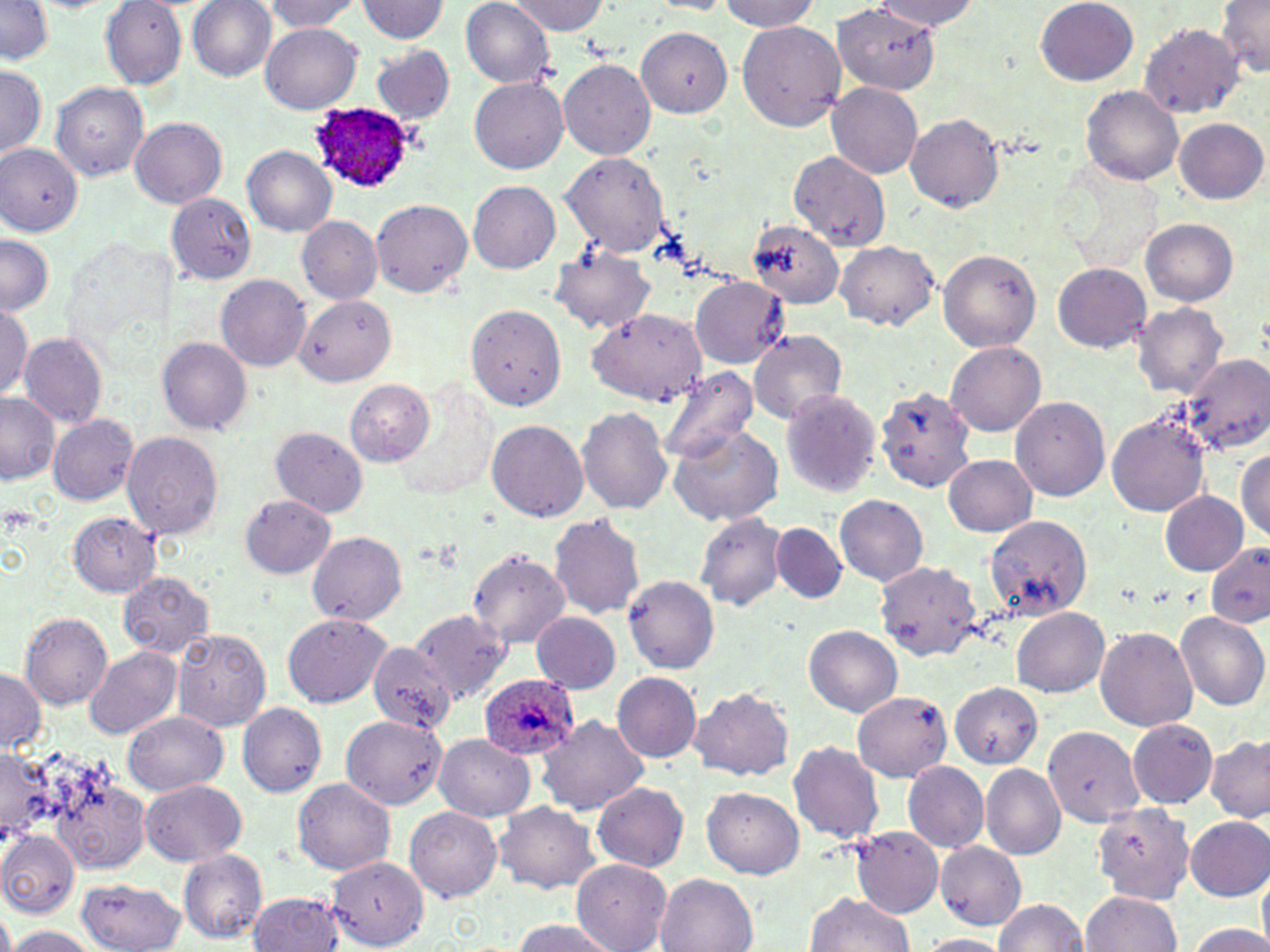

{
  "slide_level_diagnosis": "Plasmodium ovale",
  "field_of_view": "single",
  "magnification": "1000x",
  "stain": "May-Grünwald-Giemsa",
  "plasmodium_ovale_infected_red_blood_cell_locations": "approximate bounding boxes as [x1, y1, x2, y2] in pixels: [310, 102, 428, 194], [479, 674, 581, 761]",
  "modality": "optical microscopy",
  "uninfected_red_blood_cell_locations": "approximate bounding boxes as [x1, y1, x2, y2] in pixels: [99, 0, 187, 88], [263, 0, 359, 34], [507, 0, 606, 34], [721, 0, 819, 32], [870, 0, 980, 32], [1035, 0, 1139, 85], [0, 1, 54, 63], [187, 1, 276, 81], [355, 1, 448, 43], [460, 1, 557, 87], [647, 1, 730, 14], [1216, 1, 1270, 78], [833, 4, 940, 96], [737, 20, 846, 130], [1139, 22, 1244, 119], [261, 23, 361, 114], [635, 26, 732, 118], [370, 43, 456, 126], [558, 59, 655, 160], [0, 63, 45, 159], [470, 77, 568, 173], [51, 81, 149, 182], [827, 83, 922, 179], [1081, 86, 1183, 185], [905, 113, 1005, 212], [130, 117, 227, 208], [1174, 118, 1267, 204], [0, 144, 82, 235], [243, 145, 338, 237], [559, 151, 671, 258], [787, 151, 890, 249], [469, 180, 560, 273], [166, 193, 256, 284], [370, 197, 473, 297], [296, 216, 383, 305], [1140, 217, 1238, 306], [748, 219, 845, 309], [0, 234, 55, 315], [835, 242, 939, 328], [547, 244, 657, 334], [938, 249, 1042, 352], [1054, 262, 1150, 352], [217, 274, 312, 371], [691, 276, 791, 369], [296, 294, 396, 386], [0, 302, 31, 402], [1132, 302, 1229, 400], [466, 304, 566, 410], [587, 309, 707, 405], [748, 331, 848, 426], [19, 332, 109, 429], [157, 337, 253, 434], [945, 340, 1046, 436], [1177, 352, 1270, 457], [654, 365, 761, 463], [344, 378, 436, 465], [877, 383, 981, 496], [778, 388, 881, 497], [0, 392, 59, 483], [1011, 397, 1110, 500], [577, 405, 672, 516], [1105, 409, 1213, 518], [49, 413, 138, 505], [487, 418, 588, 521], [665, 423, 786, 526], [270, 425, 368, 517], [119, 430, 223, 541], [1234, 448, 1270, 544], [943, 454, 1037, 537], [1160, 491, 1247, 574], [239, 494, 336, 579], [835, 494, 928, 587], [693, 511, 791, 612], [69, 513, 161, 596], [548, 513, 645, 620], [984, 515, 1093, 618], [772, 521, 847, 603], [307, 531, 408, 626], [1205, 541, 1270, 629], [467, 548, 571, 648], [874, 561, 984, 662], [119, 571, 216, 658], [623, 574, 720, 674], [1011, 607, 1109, 697], [410, 608, 513, 704], [531, 610, 621, 695], [1173, 612, 1269, 712], [17, 613, 113, 709], [282, 613, 390, 707], [804, 625, 902, 717], [1094, 626, 1198, 730], [172, 629, 272, 732], [368, 642, 457, 735], [85, 646, 182, 739], [0, 667, 44, 753], [612, 672, 702, 762], [951, 681, 1044, 767], [687, 686, 795, 781], [853, 692, 950, 781], [237, 702, 327, 797], [122, 711, 227, 796], [341, 714, 447, 805], [537, 714, 649, 814], [1126, 718, 1219, 808], [1040, 724, 1143, 828], [433, 733, 538, 822], [1206, 735, 1270, 823], [787, 741, 885, 843], [0, 745, 52, 844], [37, 753, 150, 878], [902, 760, 989, 852], [980, 764, 1066, 859], [139, 778, 247, 865], [292, 778, 394, 874], [592, 781, 689, 873], [703, 787, 803, 879], [494, 801, 600, 894], [1088, 802, 1194, 901], [404, 804, 502, 901], [1184, 815, 1270, 900], [851, 827, 944, 918], [0, 830, 79, 918], [934, 842, 1024, 929], [177, 849, 268, 944], [326, 857, 429, 949], [571, 860, 672, 951], [1257, 869, 1270, 950], [655, 874, 758, 952], [76, 877, 186, 952], [1079, 891, 1182, 952], [247, 893, 343, 951], [805, 893, 915, 951], [994, 898, 1087, 952], [508, 919, 621, 951], [1183, 921, 1268, 952], [4, 926, 100, 951], [919, 934, 1012, 952]",
  "preparation": "thin blood film",
  "image_size": "1270×952 pixels"
}